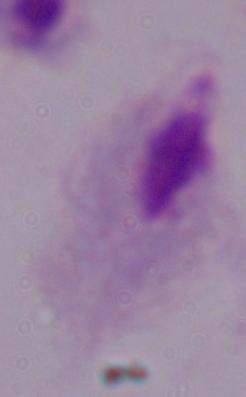 A trichomonad is seen. Captured at 1000x magnification. Micrograph.